Give the extent of the malaria parasites you find, grouped by life-cycle stage — ring form, trophozoite, schizont, or gametocyte.
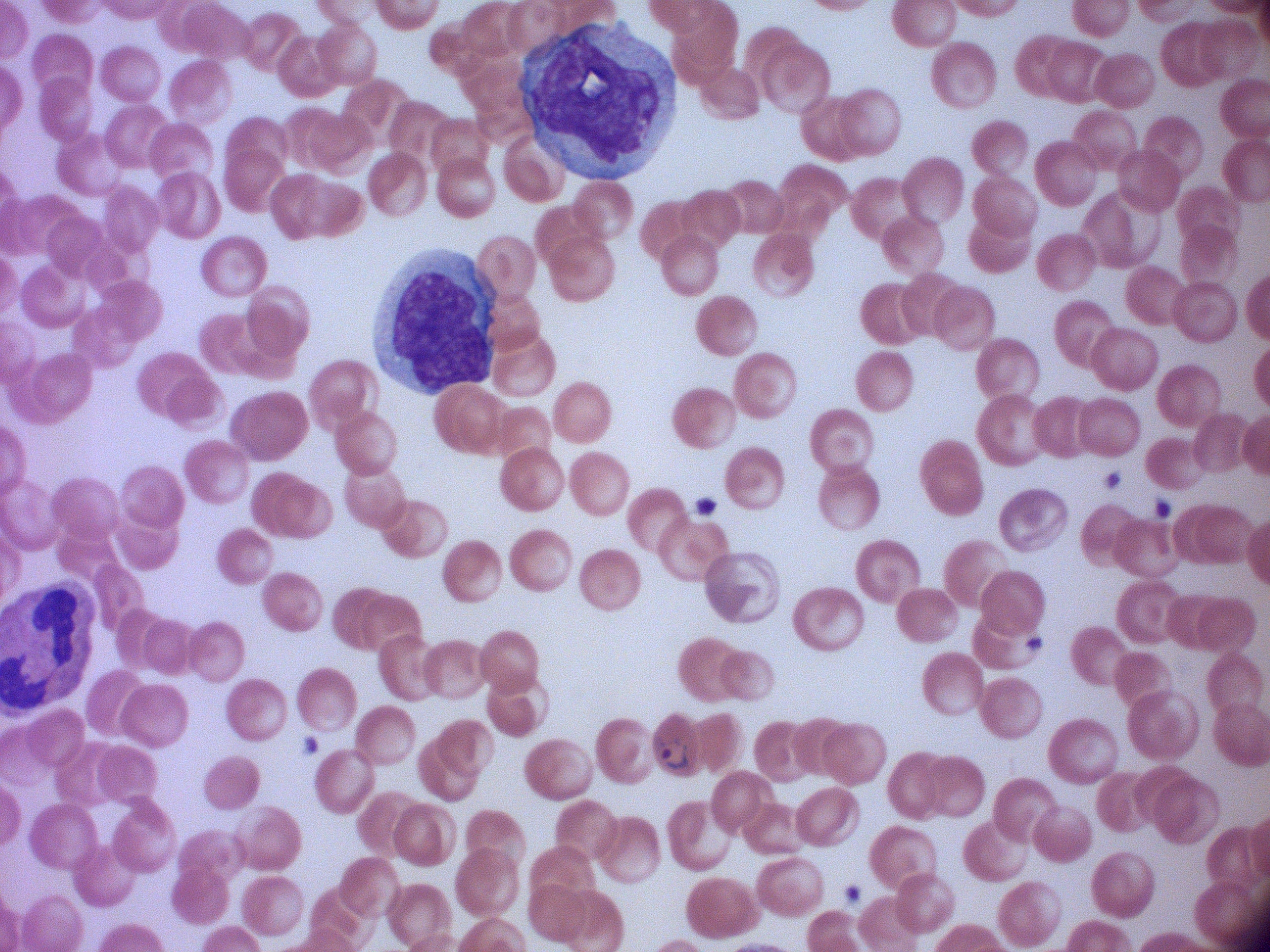

Approximate bounding boxes as (x1,y1)-(x2,y2) corner pairs in pixels, from the source annotation, which is not necessarily exhaustive.
Ring forms: (649,733)-(692,775).

{
  "image_size": "1270×952 pixels",
  "species": "Plasmodium falciparum",
  "microscope": "Leica DM2000 with built-in camera",
  "stain": "Giemsa",
  "magnification": "100x",
  "preparation": "thin blood film",
  "field_of_view": "one from this slide"
}